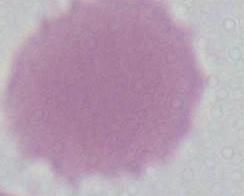
Summary:
  - Identification: erythrocyte
  - Magnification: 1000x
  - Modality: photomicrograph